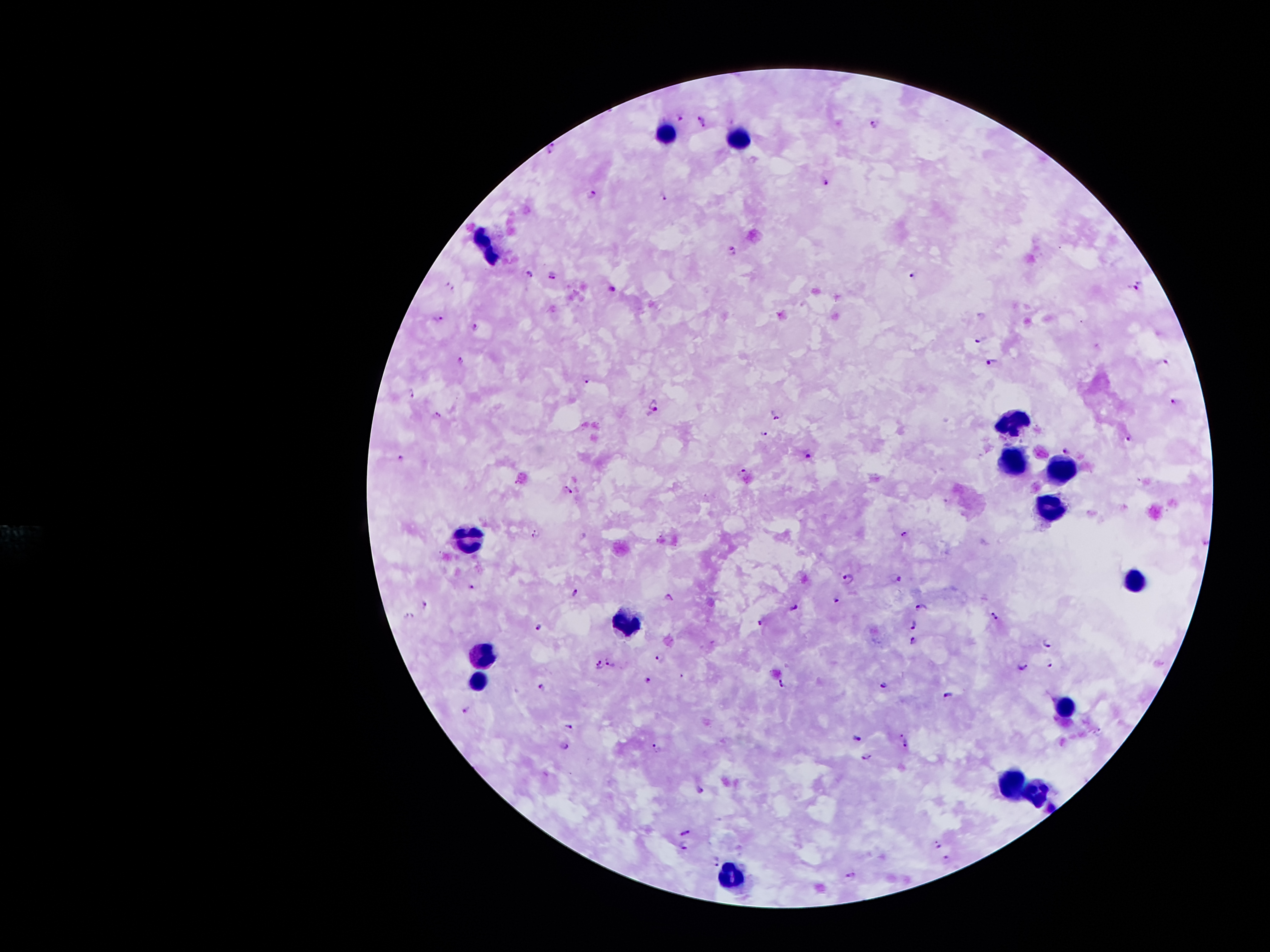

coordinate format = approximate centers as (x, y) in pixels
leukocyte locations = (663, 134), (738, 137), (487, 252), (1007, 420), (1009, 459), (1060, 464), (1051, 507), (469, 535), (1140, 582), (626, 624), (486, 654), (478, 685), (1065, 708), (1012, 784), (1040, 792), (729, 873)
Plasmodium parasite locations = (679, 118), (703, 120), (875, 123), (551, 147), (826, 182), (592, 195), (664, 198), (733, 249), (529, 274), (914, 274), (553, 275), (450, 284), (1139, 284), (614, 287), (437, 317), (476, 325), (981, 340), (462, 357), (993, 362), (1167, 363), (587, 380), (411, 393), (1175, 402), (655, 403), (440, 413), (776, 416), (764, 432), (1128, 437), (1067, 451), (807, 455), (400, 456), (744, 470), (569, 491), (536, 534), (906, 534), (1206, 542), (897, 577), (849, 579), (472, 585), (575, 592), (668, 596), (836, 601), (426, 602), (795, 606), (920, 608), (996, 615), (410, 616), (763, 621), (912, 623), (540, 628), (913, 640), (1048, 643), (660, 658), (610, 662), (1050, 663), (598, 664), (1023, 666), (649, 680), (783, 681), (883, 685), (541, 687), (946, 696), (467, 708), (569, 726), (1098, 732), (901, 734), (857, 738), (905, 744), (565, 746), (658, 748), (868, 757), (701, 790), (687, 832), (939, 841), (683, 845), (949, 859), (715, 861), (850, 876)
image size = 1270×952 pixels
magnification = 100x
field of view = one from this slide
patient malaria status = positive for Plasmodium falciparum
stain = Giemsa
capture = smartphone through the microscope eyepiece
preparation = thick blood smear